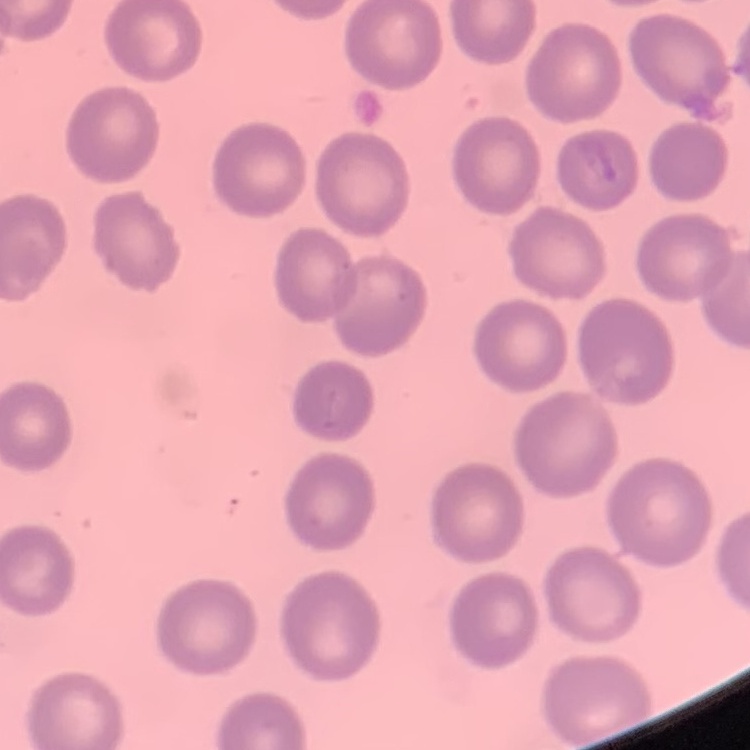
erythrocyte morphology = no rouleaux formation
preparation = thin peripheral smear
image type = square crop of a larger photomicrograph
stain = Field's or Giemsa